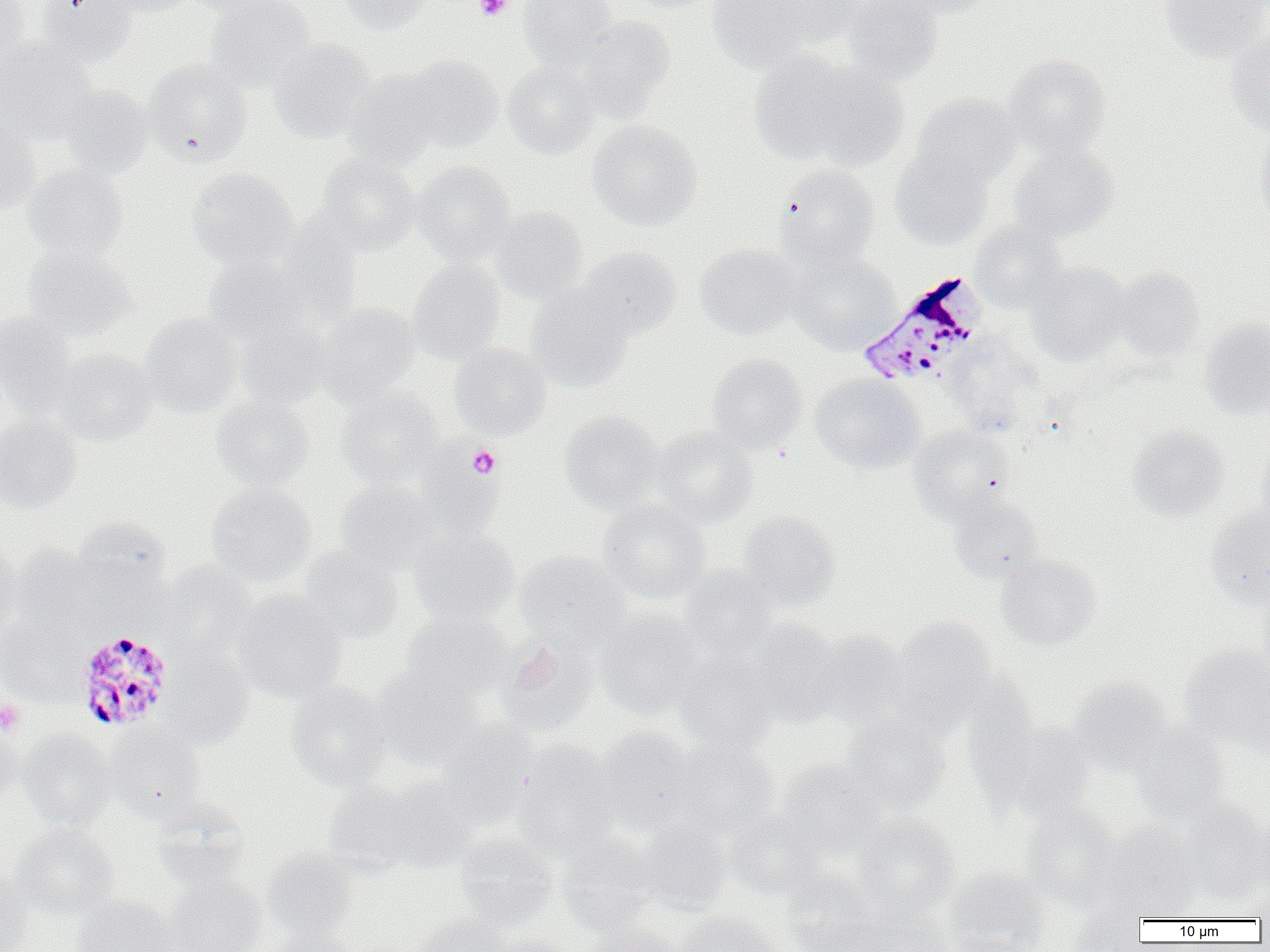
Approximate bounding boxes as [x1, y1, x2, y2] in pixels. Plasmodium malariae-infected red blood cell locations: [855, 272, 985, 386], [74, 628, 175, 732]. Uninfected red blood cell locations: [0, 0, 30, 66], [35, 0, 138, 65], [99, 0, 197, 17], [179, 0, 280, 17], [205, 0, 316, 90], [335, 0, 432, 34], [518, 0, 617, 68], [622, 0, 723, 13], [707, 0, 815, 72], [842, 0, 942, 85], [895, 0, 996, 18], [1162, 0, 1270, 63], [763, 1, 867, 49], [573, 15, 676, 116], [1227, 32, 1270, 137], [271, 39, 378, 143], [0, 40, 98, 143], [751, 51, 897, 167], [402, 54, 503, 151], [1004, 54, 1111, 156], [141, 60, 252, 165], [502, 61, 600, 159], [344, 68, 443, 168], [58, 84, 153, 179], [913, 93, 1020, 186], [0, 114, 42, 216], [589, 119, 702, 229], [1252, 126, 1270, 228], [1009, 144, 1118, 241], [890, 149, 993, 249], [318, 154, 420, 254], [411, 161, 516, 263], [23, 163, 128, 261], [776, 163, 880, 269], [186, 168, 296, 269], [489, 206, 587, 303], [970, 220, 1065, 311], [694, 244, 802, 340], [22, 245, 138, 340], [576, 247, 682, 338], [789, 252, 901, 353], [203, 258, 306, 345], [407, 259, 506, 363], [1027, 261, 1129, 363], [1114, 267, 1204, 359], [526, 287, 635, 391], [315, 303, 420, 401], [0, 312, 77, 416], [140, 313, 243, 416], [1198, 319, 1270, 420], [235, 321, 332, 410], [943, 337, 1043, 437], [450, 343, 552, 439], [54, 348, 158, 446], [707, 354, 808, 454], [811, 374, 925, 473], [336, 387, 444, 487], [211, 394, 314, 491], [559, 410, 665, 513], [0, 416, 83, 513], [653, 425, 759, 526], [908, 425, 1014, 521], [1126, 425, 1229, 521], [1257, 442, 1270, 533], [418, 447, 501, 538], [333, 481, 438, 572], [205, 483, 317, 586], [950, 496, 1044, 583], [598, 499, 710, 602], [1205, 505, 1270, 606], [738, 510, 841, 608], [74, 517, 171, 599], [409, 528, 519, 627], [0, 543, 20, 643], [9, 543, 104, 634], [298, 547, 404, 643], [515, 550, 627, 648], [997, 554, 1100, 649], [159, 562, 256, 658], [679, 565, 777, 656], [1257, 582, 1270, 681], [233, 590, 347, 703], [597, 611, 703, 719], [400, 612, 513, 703], [894, 617, 996, 723], [0, 619, 83, 704], [750, 619, 840, 726], [811, 630, 910, 726], [495, 635, 599, 737], [1179, 643, 1270, 750], [161, 648, 255, 748], [675, 651, 776, 754], [373, 669, 487, 768], [962, 673, 1039, 804], [1070, 676, 1173, 772], [1241, 680, 1270, 761], [287, 683, 394, 790], [840, 712, 950, 815], [437, 720, 538, 827], [1000, 720, 1098, 823], [0, 721, 24, 807], [1132, 723, 1233, 822], [105, 724, 206, 820], [598, 726, 696, 833], [18, 729, 116, 830], [513, 741, 620, 858], [673, 741, 779, 838], [776, 759, 888, 856], [379, 778, 477, 873], [323, 780, 423, 873], [150, 799, 252, 890], [1180, 801, 1269, 903], [1020, 804, 1122, 910], [726, 811, 827, 899], [852, 811, 961, 918], [636, 822, 732, 914], [11, 823, 119, 919], [1099, 823, 1204, 916], [453, 833, 558, 929], [556, 834, 661, 934], [262, 846, 359, 941], [945, 867, 1049, 952], [0, 869, 32, 952], [781, 872, 885, 951], [164, 873, 268, 952], [1242, 883, 1270, 921], [71, 895, 179, 952], [852, 902, 953, 952], [1067, 907, 1147, 951], [672, 910, 782, 952], [410, 913, 509, 952], [583, 923, 685, 952], [267, 927, 365, 952], [484, 932, 574, 952]. Platelet locations: [474, 0, 512, 21], [448, 441, 506, 489], [467, 444, 501, 479], [0, 700, 26, 736]. Slide-level diagnosis: Plasmodium malariae. Captured at 1000x magnification. Optical microscopy. Thin blood smear. Image is 1270×952 pixels. One field of a larger specimen.